Assess this cell for malaria.
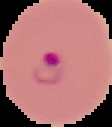
Parasitized.

preparation = thin blood smear
image size = 112×127 pixels
image type = segmented cell region on a black background